Locate every Plasmodium ovale-infected red blood cell.
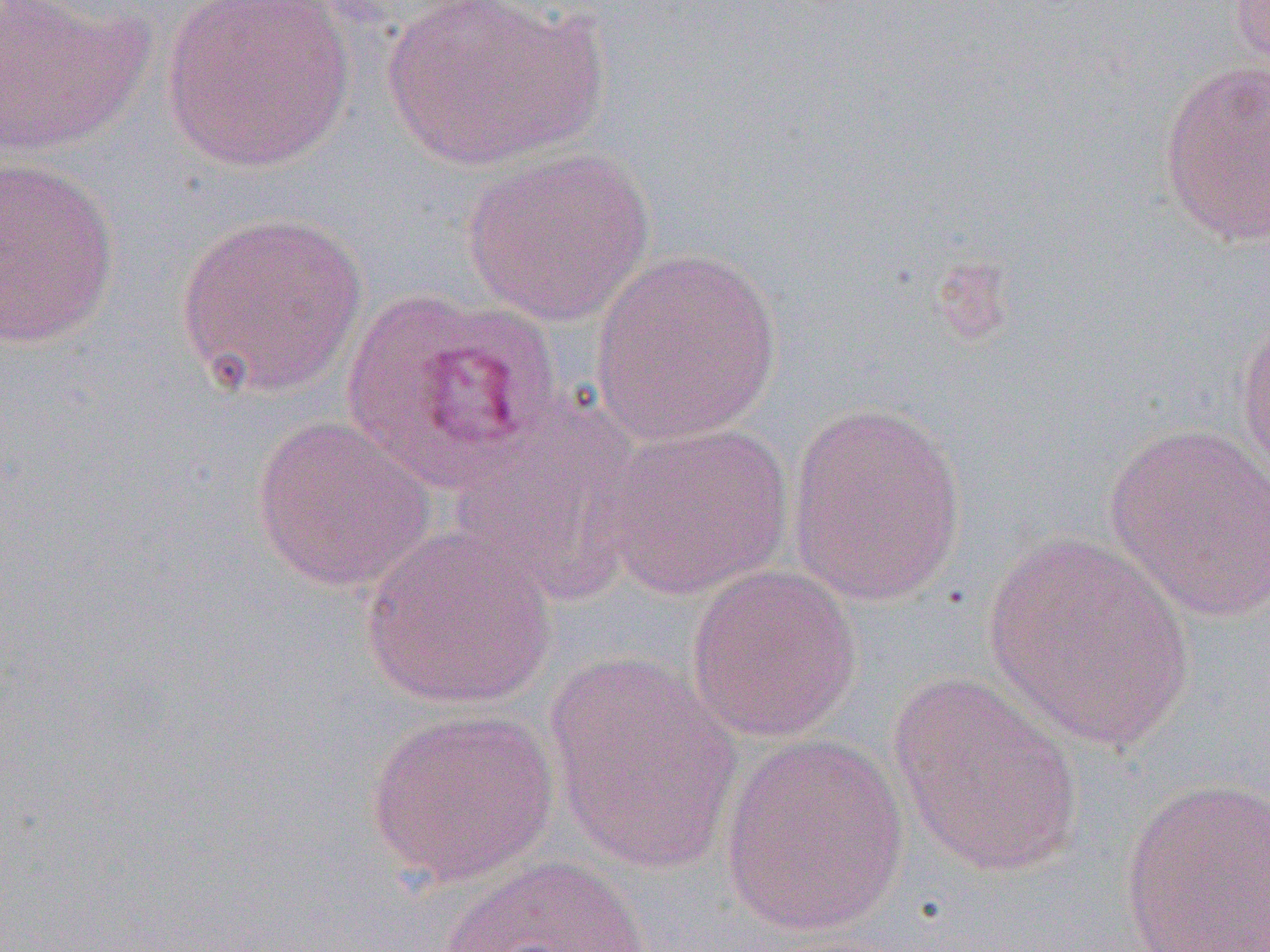

Approximate bounding boxes as (x1, y1, x2, y2) in pixels.
Plasmodium ovale-infected red blood cells: (340, 286, 566, 491).

Uninfected red blood cell locations: (0, 0, 152, 157), (161, 0, 356, 175), (378, 0, 610, 170), (1228, 0, 1270, 74), (1158, 58, 1270, 247), (460, 146, 656, 327), (1, 155, 121, 349), (174, 210, 370, 399), (588, 247, 784, 446), (1233, 308, 1270, 489), (786, 400, 969, 607), (446, 401, 646, 603), (250, 413, 437, 594), (596, 420, 795, 602), (1103, 423, 1270, 625), (361, 528, 557, 710), (982, 531, 1197, 752), (684, 563, 862, 744), (544, 652, 743, 875), (888, 671, 1086, 878), (364, 708, 559, 886), (718, 733, 910, 938), (1118, 776, 1270, 951), (437, 852, 655, 952). Slide-level diagnosis: Plasmodium ovale. Single field of view. Thin blood film. 1000x magnification. Image is 1270×952 pixels. Light microscopy.